Locate every Plasmodium falciparum-infected red blood cell.
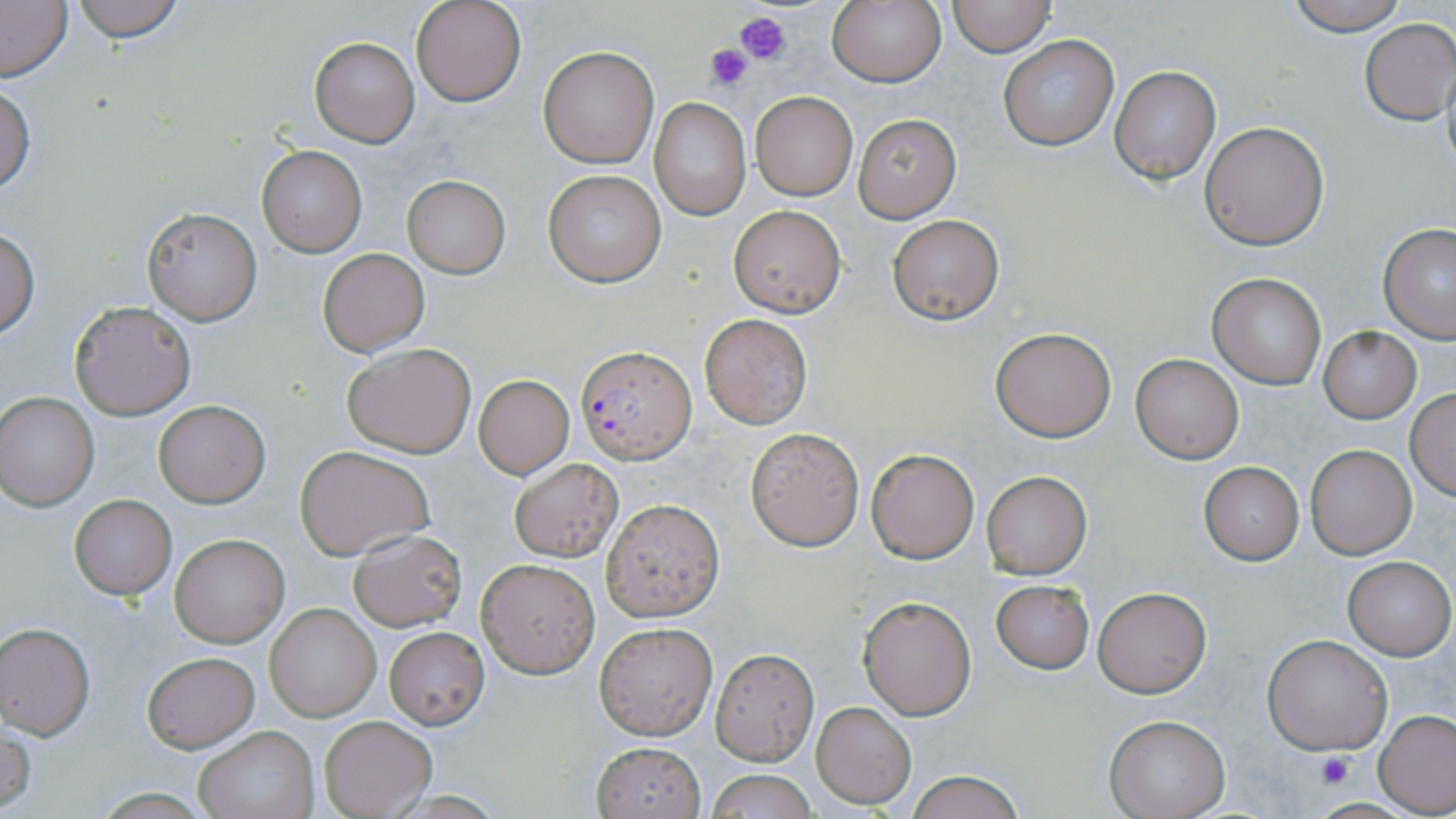
Approximate bounding boxes as (x1, y1, x2, y2) in pixels.
Plasmodium falciparum-infected red blood cells: (577, 345, 695, 463).

Summary:
  - Uninfected red blood cell locations: (68, 0, 187, 43), (411, 0, 526, 107), (827, 0, 944, 88), (947, 0, 1056, 56), (1284, 0, 1410, 35), (0, 1, 73, 83), (1359, 19, 1455, 124), (997, 34, 1118, 151), (310, 37, 419, 148), (537, 46, 659, 168), (1110, 65, 1221, 184), (0, 83, 36, 196), (750, 92, 859, 201), (650, 98, 751, 220), (853, 114, 960, 222), (1199, 121, 1329, 251), (257, 146, 367, 258), (543, 169, 667, 286), (401, 176, 510, 277), (728, 206, 846, 317), (143, 208, 261, 325), (887, 213, 1005, 326), (1378, 223, 1456, 343), (0, 229, 38, 339), (319, 248, 428, 355), (1207, 272, 1327, 389), (69, 302, 195, 419), (699, 314, 812, 427), (989, 326, 1118, 443), (1317, 327, 1421, 422), (342, 343, 476, 458), (1131, 354, 1243, 463), (473, 374, 575, 479), (1405, 388, 1456, 501), (0, 393, 99, 510), (153, 401, 269, 507), (745, 427, 865, 551), (293, 444, 435, 560), (1306, 444, 1415, 557), (864, 447, 979, 563), (509, 456, 624, 563), (1198, 462, 1304, 565), (981, 470, 1092, 578), (69, 495, 176, 599), (601, 498, 725, 621), (347, 528, 467, 631), (170, 534, 288, 646), (1343, 556, 1455, 660), (476, 558, 600, 677), (990, 578, 1095, 674), (1092, 585, 1212, 698), (858, 595, 976, 720), (265, 602, 380, 721), (594, 621, 717, 739), (0, 622, 95, 738), (383, 626, 490, 729), (1263, 635, 1393, 755), (710, 648, 819, 765), (142, 652, 259, 752), (812, 702, 915, 809), (1375, 710, 1456, 815), (318, 714, 435, 818), (1105, 716, 1228, 818), (1, 719, 36, 815), (193, 725, 319, 819), (592, 742, 705, 818), (707, 767, 817, 819), (903, 770, 1029, 819)
  - Platelet locations: (735, 10, 790, 65), (706, 42, 755, 91), (1316, 751, 1352, 788)
  - Slide-level diagnosis: Plasmodium falciparum
  - Preparation: thin blood film
  - Stain: May-Grünwald-Giemsa
  - Field of view: one of a larger specimen
  - Image size: 1456×819 pixels
  - Magnification: 1000x
  - Modality: light microscopy